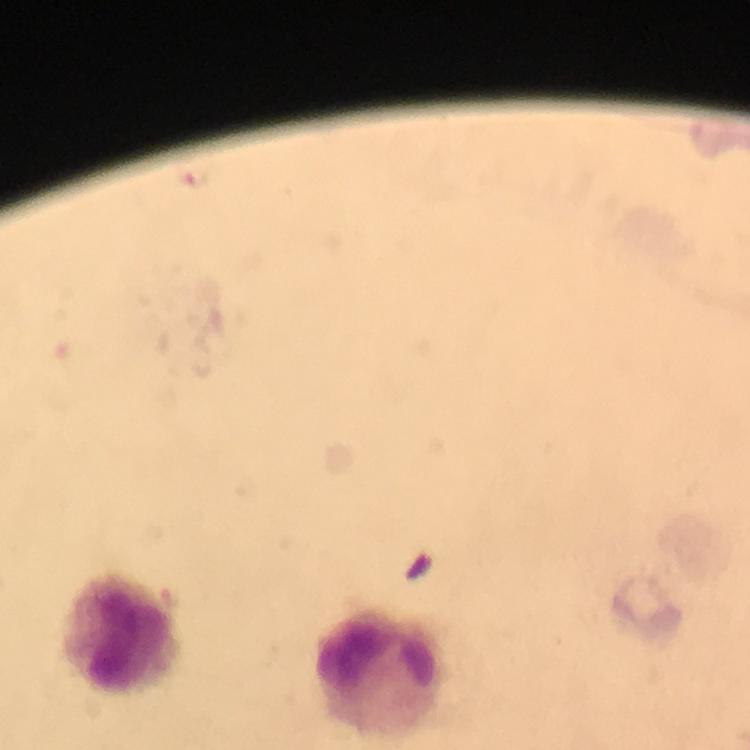
immersion oil = used
Plasmodium parasite locations = approximate centers as [x, y] in pixels: [194, 177]
image size = 750×750 pixels
stain = Giemsa
cropped from = one field of view
magnification = 100x
context = from a malaria diagnostic workup
leukocyte locations = approximate centers as [x, y] in pixels: [121, 635], [382, 670]
preparation = thick blood film
capture = smartphone photograph through a microscope